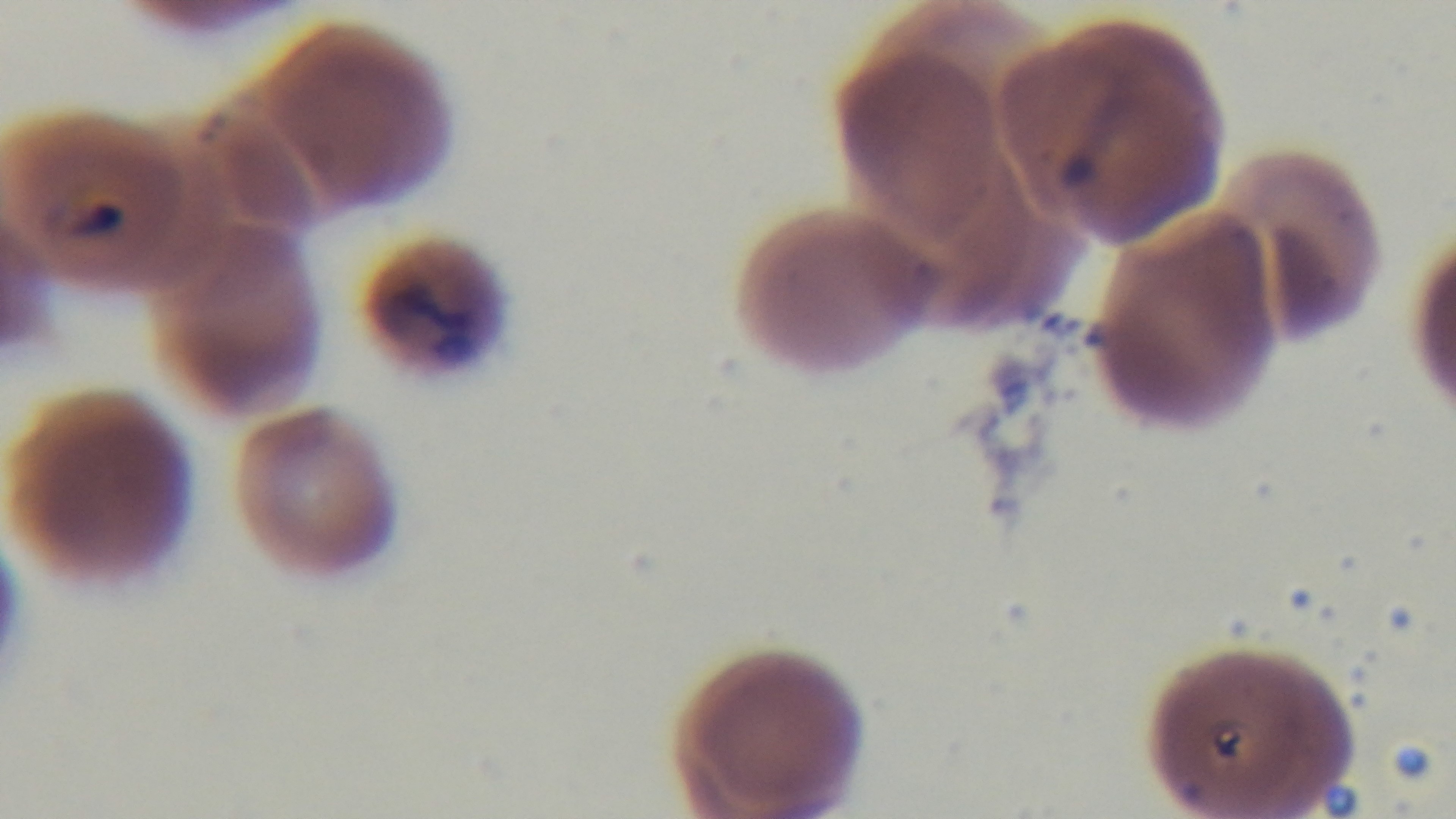
malaria_status: positive
field_of_view: one from the slide
modality: light microscopy
stain: Giemsa
preparation: thin
objective: 100x oil immersion
capture: mounted 4K digital camera